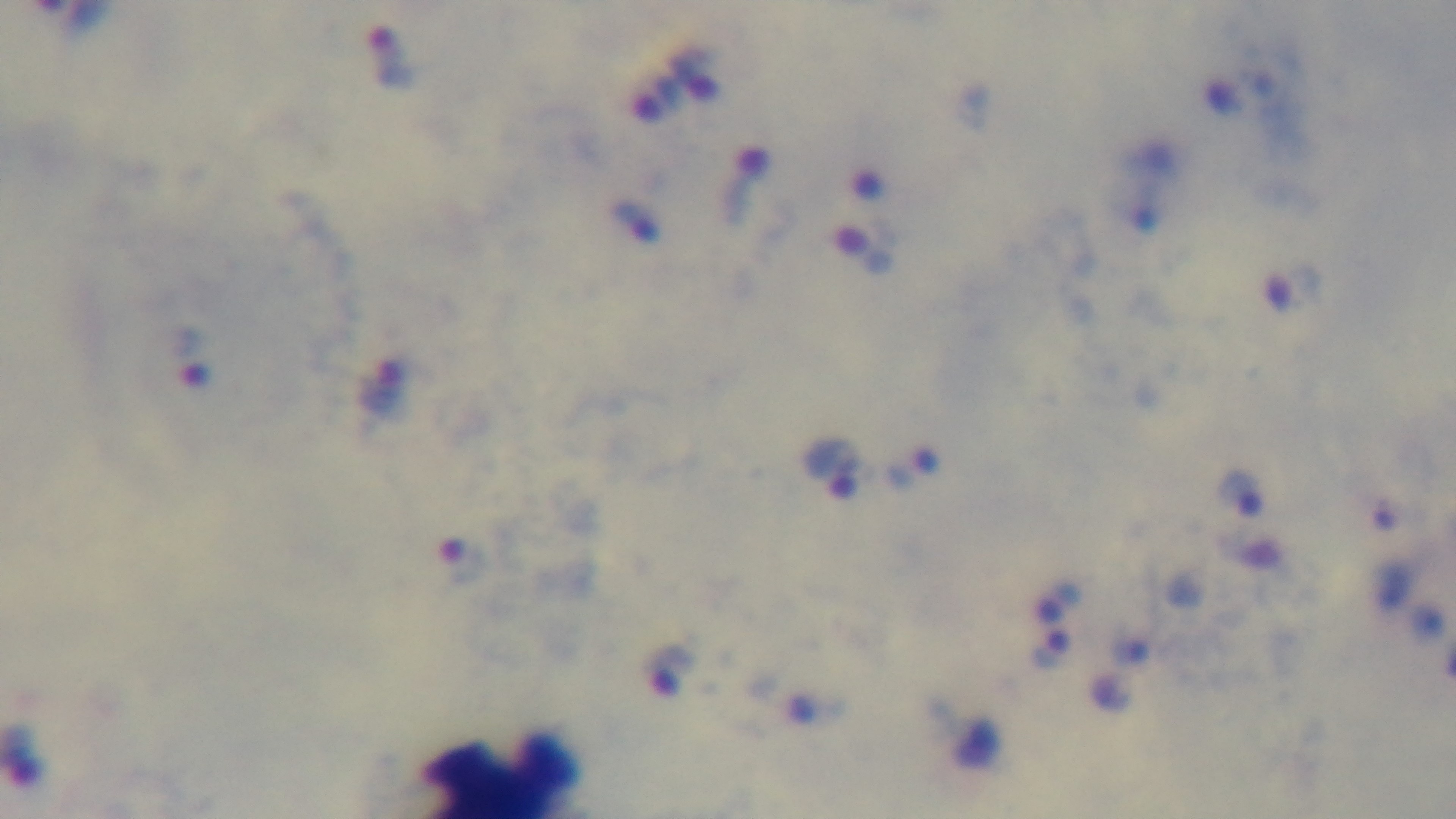 Preparation: thick smear. Giemsa-stained. Malaria status: infected. 100x oil-immersion objective. Photomicrograph. Mounted 4K digital camera. One field from the slide.